Classify this cell by malaria status.
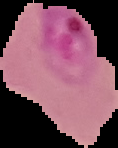

Parasitized.

From a thin blood film. The area outside the segmented cell region is set to black. Image is 118×148 pixels.